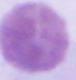
Summary:
  - Identification: red blood cell
  - Modality: photomicrograph
  - Magnification: 1000x